Locate every blood parasite and identify its species.
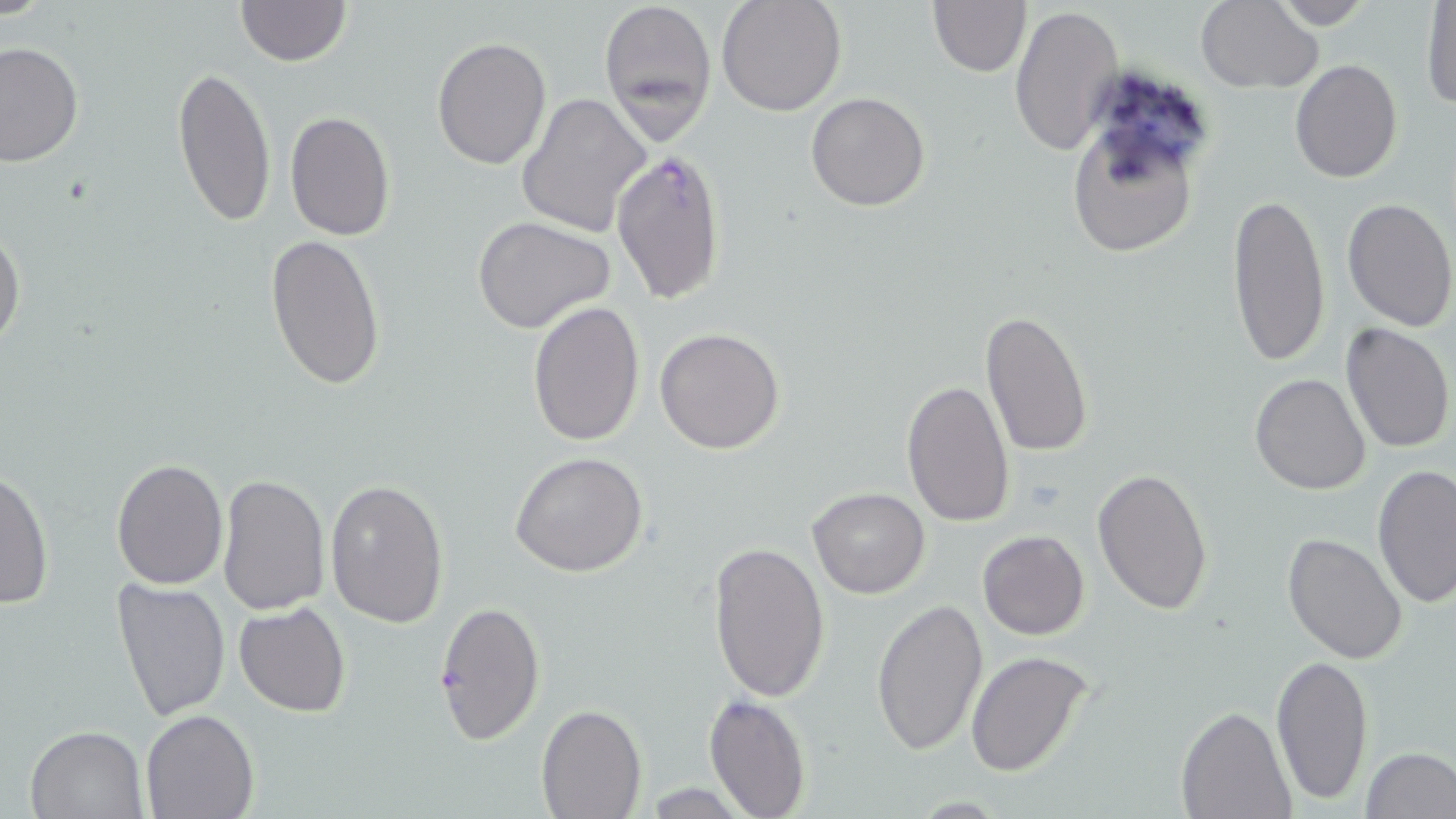

Approximate bounding boxes as [x1, y1, x2, y2] in pixels.
Plasmodium falciparum-infected red blood cells: [610, 147, 729, 302], [434, 600, 546, 745].
No Plasmodium ovale, Plasmodium malariae, Plasmodium vivax, Babesia divergens, or Trypanosoma brucei observed.

slide-level diagnosis = Plasmodium falciparum
field of view = one of a larger specimen
uninfected red blood cell locations = approximate bounding boxes as [x1, y1, x2, y2] in pixels: [235, 0, 351, 67], [600, 0, 718, 142], [717, 0, 847, 117], [1270, 0, 1375, 28], [927, 1, 1030, 77], [1193, 1, 1322, 93], [1421, 1, 1455, 112], [1009, 2, 1123, 158], [431, 37, 552, 169], [0, 41, 84, 169], [1290, 59, 1402, 183], [172, 63, 277, 229], [517, 92, 652, 238], [805, 92, 930, 211], [1066, 107, 1206, 263], [283, 111, 396, 242], [1227, 189, 1333, 369], [1341, 197, 1456, 331], [472, 216, 620, 335], [0, 223, 26, 354], [264, 231, 386, 391], [527, 300, 644, 447], [978, 309, 1094, 457], [1339, 322, 1455, 452], [656, 327, 785, 454], [1249, 373, 1371, 494], [901, 379, 1015, 525], [510, 452, 649, 577], [111, 459, 227, 589], [1373, 465, 1455, 606], [0, 466, 53, 610], [1092, 469, 1214, 615], [216, 473, 333, 617], [324, 479, 450, 627], [808, 487, 929, 598], [977, 530, 1090, 639], [1281, 532, 1407, 665], [708, 540, 830, 703], [110, 579, 232, 724], [872, 597, 990, 755], [234, 602, 351, 717], [964, 649, 1095, 777], [1270, 651, 1372, 805], [703, 691, 810, 818], [536, 703, 646, 817], [1177, 706, 1295, 819], [140, 711, 259, 819], [24, 725, 149, 817], [1362, 746, 1456, 818]
magnification = 1000x
modality = optical microscopy
image size = 1456×819 pixels
preparation = thin blood film
stain = May-Grünwald-Giemsa